Find the red blood cells that are infected with P. falciparum, and any of indeterminate infection status.
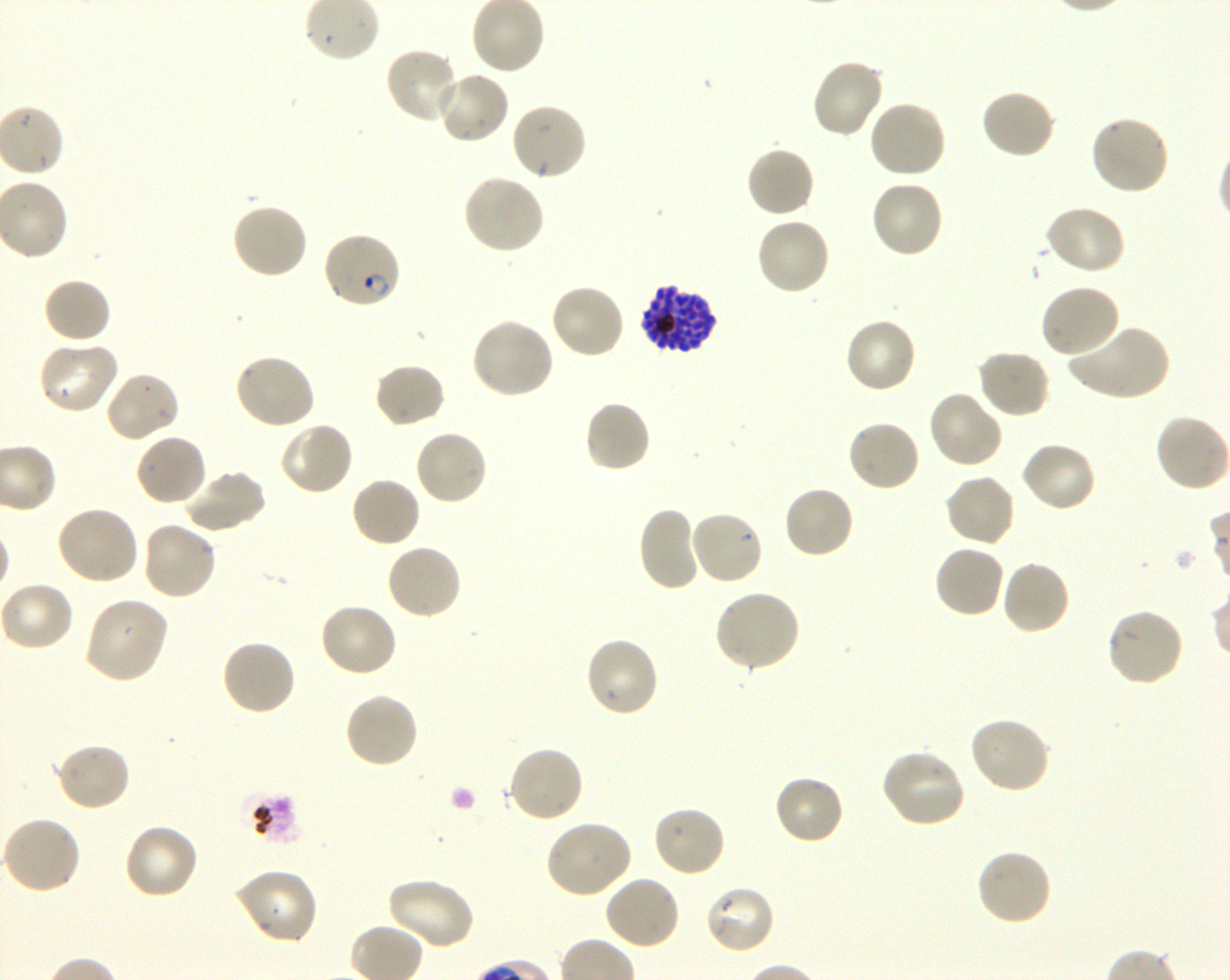
Approximate bounding boxes as (x1, y1, x2, y2) in pixels. Not every red blood cell is marked. A life-cycle stage — or a range of stages, where the recorded stages span more than one — follows each staged infected red blood cell.
Infected red blood cells: (322, 229, 401, 310) ring; (638, 283, 718, 355) late schizont.
No red blood cells of indeterminate infection status observed.

locations of uninfected red blood cells = (385, 46, 460, 124), (810, 58, 886, 140), (434, 71, 510, 145), (979, 88, 1056, 160), (867, 100, 946, 180), (510, 101, 589, 182), (1090, 114, 1171, 197), (745, 145, 816, 219), (461, 173, 545, 256), (870, 179, 944, 259), (231, 201, 309, 279), (1043, 204, 1126, 275), (754, 217, 831, 297), (42, 277, 112, 345), (549, 282, 626, 359), (1039, 283, 1122, 358), (470, 317, 555, 399), (842, 317, 917, 395), (1067, 325, 1174, 401), (36, 340, 121, 416), (976, 349, 1051, 419), (233, 353, 316, 431), (372, 362, 447, 430), (103, 370, 181, 444), (928, 390, 1004, 470), (583, 399, 652, 473), (1154, 413, 1230, 493), (846, 418, 922, 492), (278, 422, 354, 496), (413, 428, 489, 507), (134, 433, 209, 507), (1019, 440, 1098, 513), (181, 468, 267, 535), (943, 473, 1016, 548), (350, 476, 422, 549), (782, 484, 855, 560), (54, 503, 140, 585), (637, 506, 703, 592), (688, 509, 765, 587), (140, 521, 218, 601), (385, 543, 463, 621), (933, 544, 1005, 619), (1000, 559, 1071, 636), (0, 581, 74, 652), (713, 589, 802, 673), (84, 596, 170, 684), (317, 602, 399, 678), (1106, 608, 1185, 688), (584, 636, 661, 719), (220, 639, 298, 717), (343, 690, 420, 769), (969, 715, 1052, 795), (52, 741, 131, 813), (505, 744, 584, 824), (879, 747, 967, 828), (773, 773, 845, 845), (652, 805, 728, 878), (1, 816, 82, 895), (544, 819, 633, 899), (123, 823, 201, 901), (975, 847, 1054, 927), (232, 868, 319, 945), (603, 874, 681, 951), (384, 876, 475, 950), (703, 884, 777, 955)
life-cycle stages observed = ring, schizont
stain = Giemsa
image size = 1230×980 pixels
donor blood group = O+
objective = 100x, oil immersion, numerical aperture 1.30
culture = in-vitro P. falciparum strain 3D7, shaking
preparation = thin blood smear
field of view = one from this slide